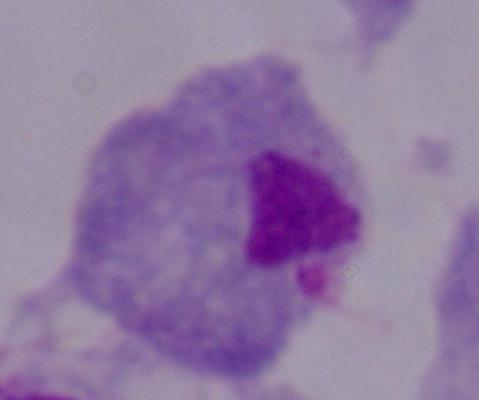

Photomicrograph. A trichomonad is seen. 1000x magnification.